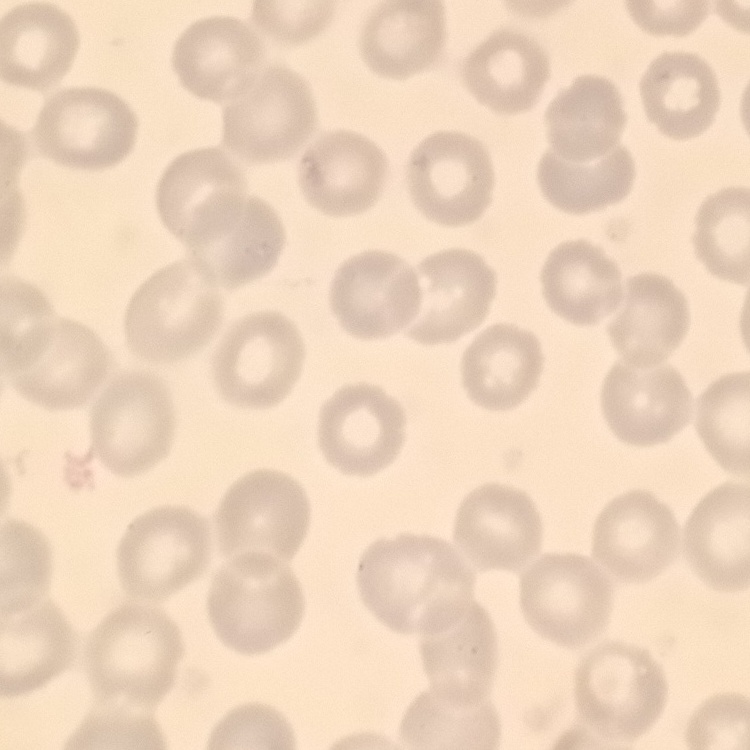
{
  "red_blood_cell_morphology": "no rouleaux formation",
  "image_type": "one tile cut from a larger photomicrograph",
  "preparation": "thin blood film",
  "stain": "Field's or Giemsa"
}